Name the parasite shown.
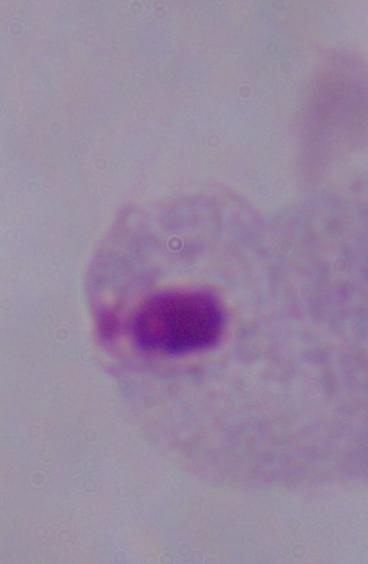
This is a trichomonad.

Summary:
  - Modality: photomicrograph
  - Magnification: 1000x